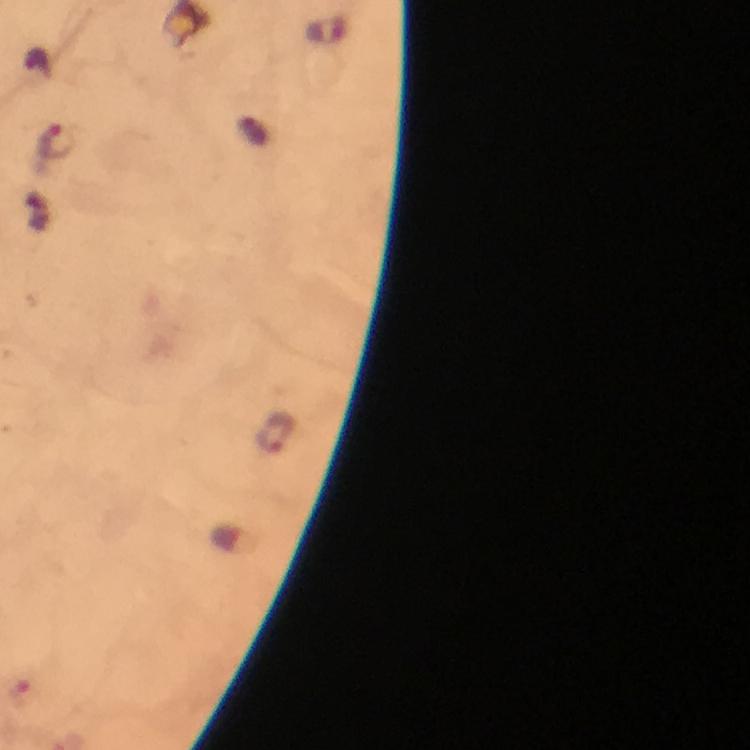

Approximate centers as (x, y) in pixels. Malaria parasite locations: (56, 141), (277, 430). 100x magnification. Image is 750×750 pixels. From a diagnostic examination for malaria. Immersion oil applied. Thick smear. Photographed with a smartphone mounted on the microscope. Cropped region of a single field of view. Giemsa stain.